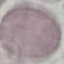
Summary:
  - Malaria status: uninfected
  - Preparation: thin smear
  - Stain: Giemsa
  - Capture: smartphone through the microscope eyepiece
  - Image type: cell patch, automatically extracted from a larger field of view and resized to 64 × 64 pixels